Report the malaria status of this cell.
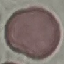
Uninfected.

Summary:
  - Capture: smartphone through the microscope eyepiece
  - Stain: Giemsa
  - Preparation: thin blood film
  - Image type: cell patch, automatically extracted from a larger field of view and resized to 64 × 64 pixels